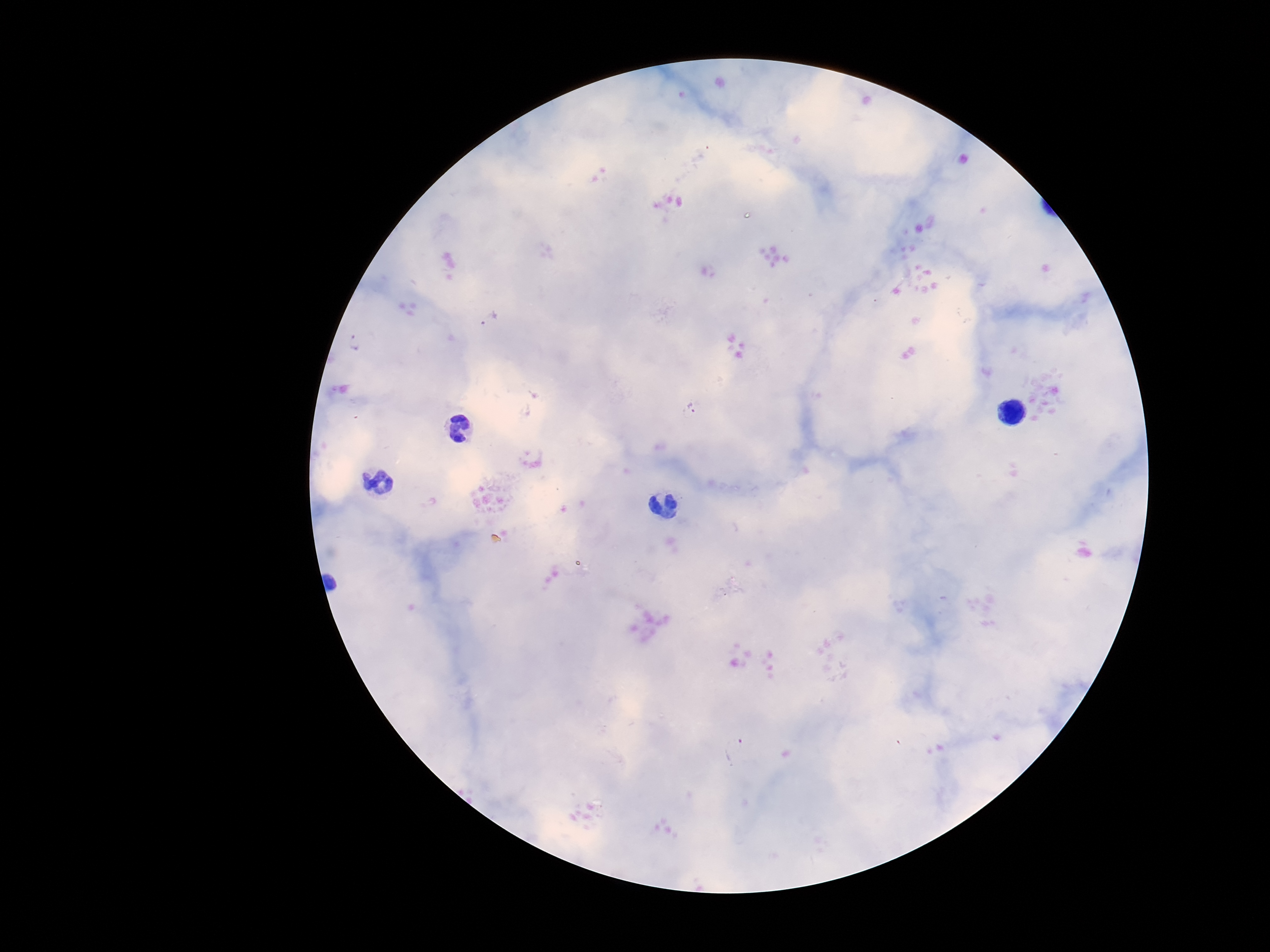

Approximate centers as [x, y] in pixels.
Summary:
  - Plasmodium parasite locations: [489, 318], [357, 343], [691, 409], [736, 749]
  - Field of view: single
  - Magnification: 100x
  - Preparation: thick peripheral-blood smear
  - Capture: smartphone camera through the microscope eyepiece
  - Patient malaria status: infected
  - Stain: Giemsa
  - Image size: 1270×952 pixels